Locate every Plasmodium parasite.
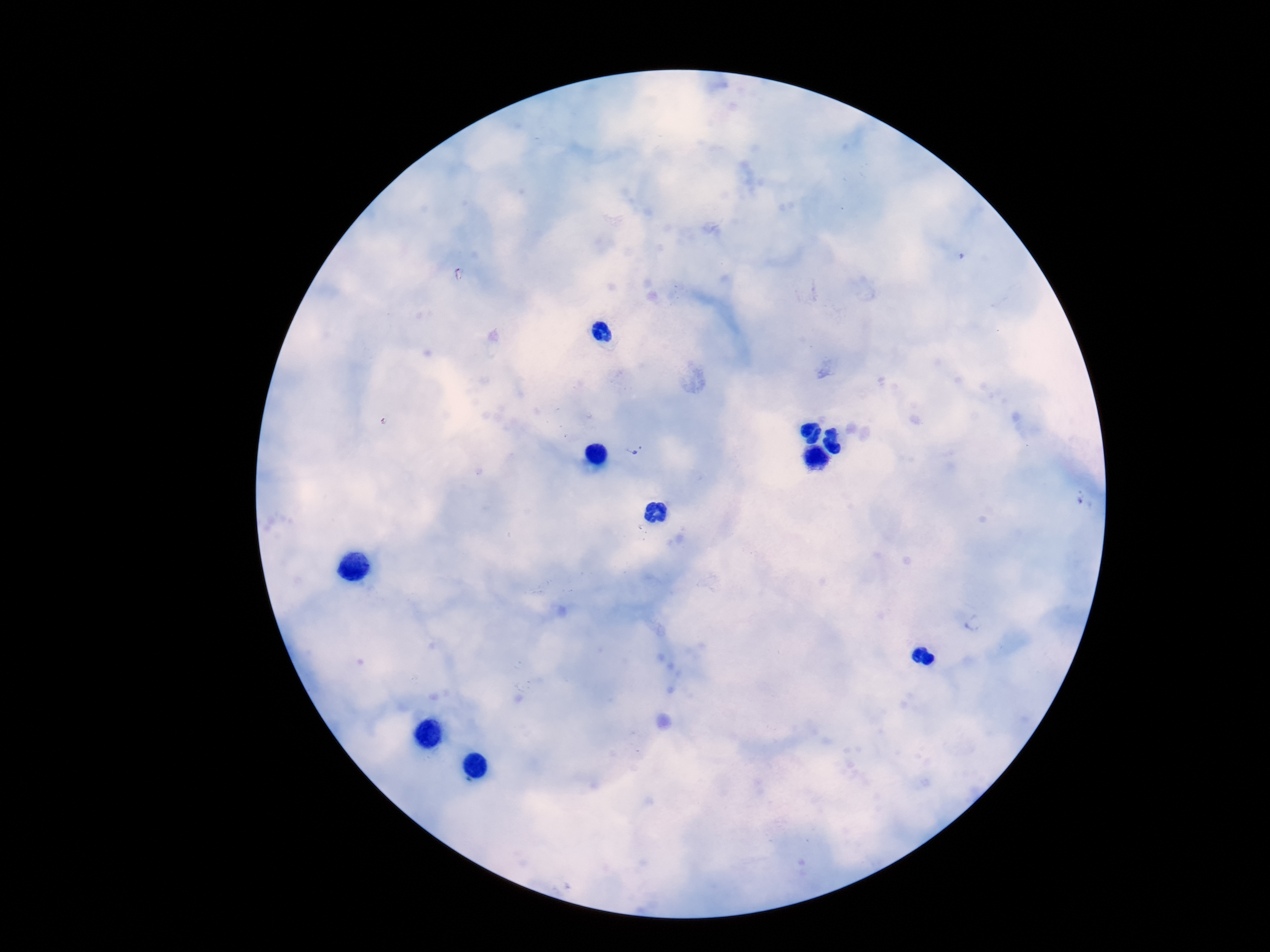
Approximate centers as [x, y] in pixels.
Plasmodium parasites: [636, 449].

Summary:
  - Preparation: thick blood smear
  - Image size: 1270×952 pixels
  - Field of view: single
  - Patient malaria status: infected
  - Stain: Giemsa
  - Capture: smartphone camera through the microscope eyepiece
  - Magnification: 100x